State the blood parasite species.
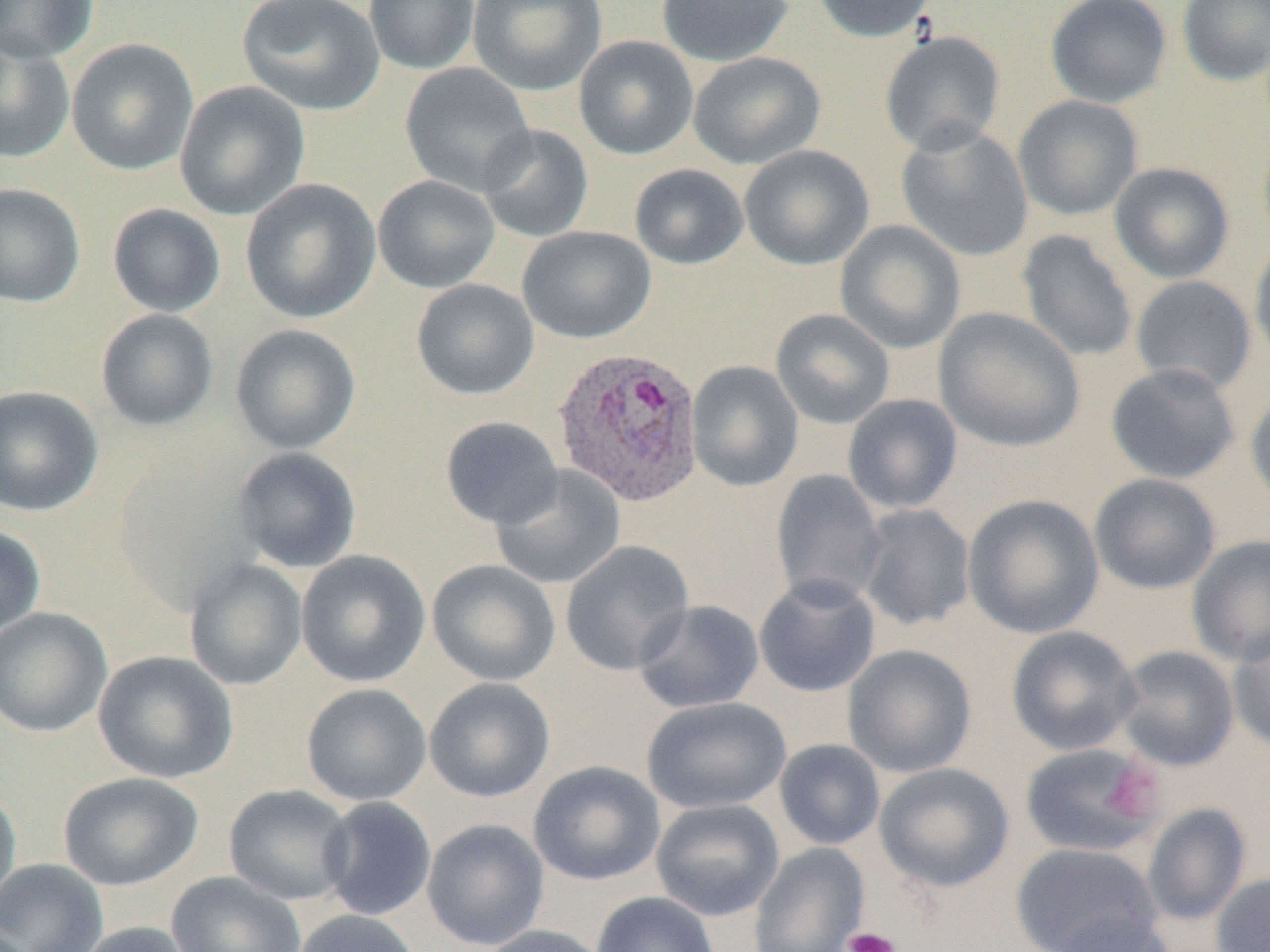
Plasmodium ovale.

Approximate bounding boxes as (x1,y1)-(x2,y2) corner pairs in pixels. Plasmodium ovale-infected red blood cell locations: (553,345)-(705,507). Platelet locations: (1106,761)-(1166,823), (843,926)-(902,952). Uninfected red blood cell locations: (0,0)-(98,63), (236,0)-(385,116), (363,0)-(481,75), (468,0)-(607,96), (655,0)-(795,66), (811,0)-(939,43), (1045,0)-(1172,108), (1177,0)-(1270,86), (879,31)-(1006,155), (0,36)-(75,165), (573,36)-(698,159), (66,38)-(198,175), (687,51)-(826,169), (399,62)-(536,196), (174,81)-(310,221), (1012,95)-(1144,221), (476,123)-(594,243), (895,123)-(1034,262), (1256,128)-(1270,255), (739,145)-(875,271), (1108,162)-(1235,284), (629,163)-(749,269), (372,175)-(500,293), (240,177)-(381,324), (0,182)-(86,308), (107,203)-(226,318), (834,220)-(966,355), (516,226)-(656,344), (1017,229)-(1138,363), (1249,236)-(1270,371), (1130,275)-(1257,395), (411,279)-(539,400), (934,307)-(1085,453), (95,309)-(219,432), (771,309)-(895,430), (230,324)-(361,455), (685,361)-(804,492), (1106,362)-(1241,484), (0,385)-(104,517), (1246,387)-(1270,515), (842,394)-(963,514), (440,416)-(564,529), (231,447)-(362,574), (491,466)-(625,590), (770,470)-(887,608), (1088,473)-(1221,594), (962,493)-(1104,640), (856,503)-(975,631), (0,524)-(46,639), (1187,535)-(1270,668), (560,540)-(695,676), (296,550)-(432,688), (184,558)-(307,691), (427,559)-(561,687), (754,574)-(881,697), (633,599)-(764,714), (0,607)-(113,737), (1007,625)-(1142,756), (1227,625)-(1270,753), (843,644)-(977,778), (1114,645)-(1240,771), (93,651)-(238,784), (423,677)-(555,803), (301,683)-(432,806), (642,696)-(791,815), (774,739)-(886,851), (1019,742)-(1165,858), (528,760)-(665,886), (874,762)-(1015,892), (58,772)-(204,891), (224,784)-(356,905), (0,787)-(21,909), (318,797)-(437,921), (651,798)-(784,921), (1142,803)-(1252,927), (422,818)-(550,951), (1010,842)-(1162,952), (748,843)-(870,952), (0,858)-(108,952), (166,871)-(307,952), (1210,872)-(1270,952), (591,891)-(720,952), (290,909)-(423,952), (1050,914)-(1180,952), (74,921)-(198,952), (478,924)-(610,952). Captured at 1000x magnification. Light microscopy. One field of a larger specimen. Image is 1270×952 pixels. Thin blood film.